Identify the preparation type.
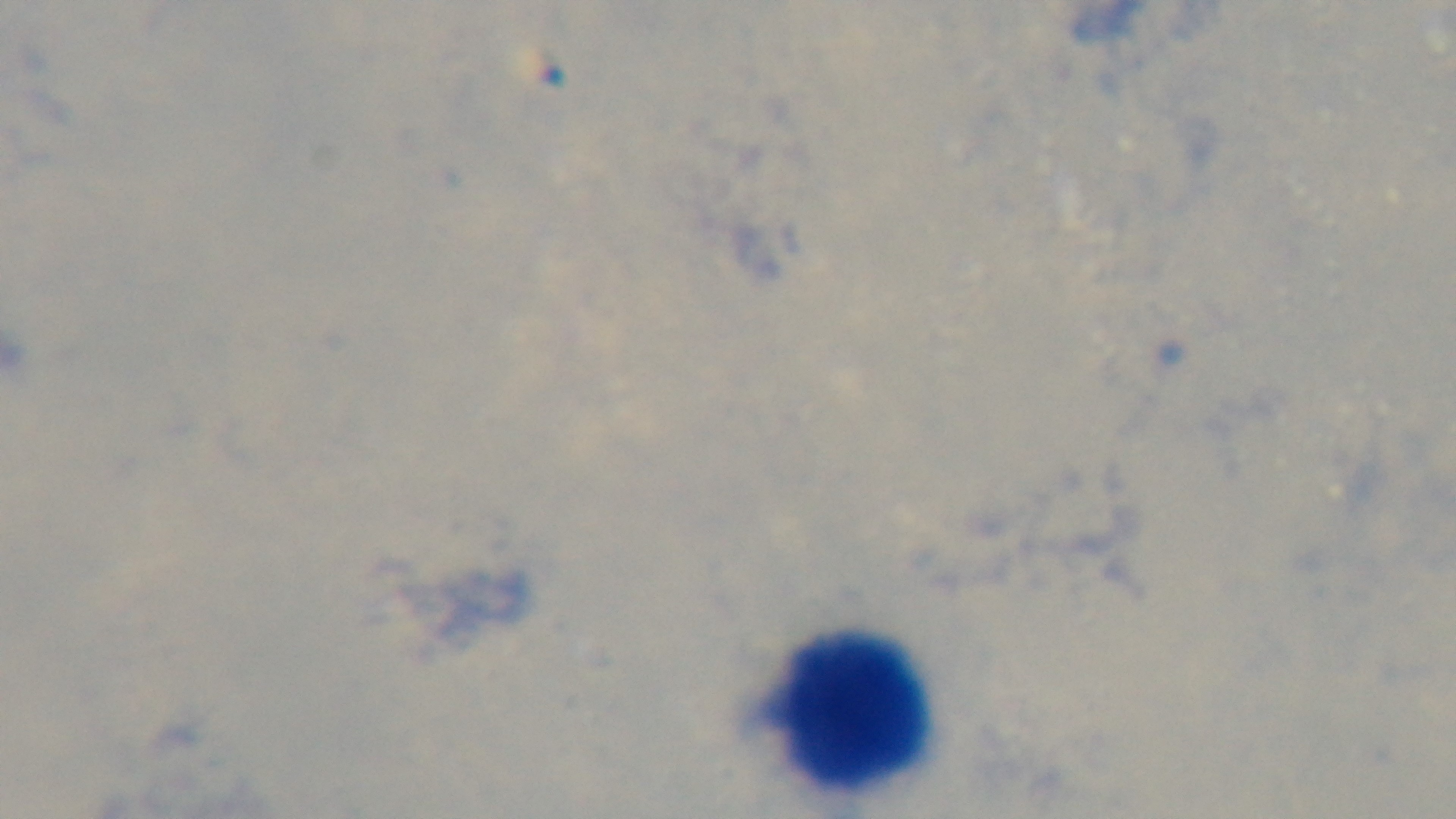

It is a thick blood film.

Summary:
  - Objective: 100x oil immersion
  - Malaria status: uninfected
  - Capture: mounted 4K digital camera
  - Field of view: one from the slide
  - Stain: Giemsa
  - Modality: light microscopy